Name the cell type shown.
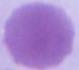

This is an erythrocyte.

Micrograph. Captured at 1000x magnification.